Assess this cell for malaria.
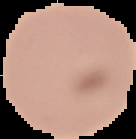

Uninfected.

Summary:
  - Preparation: thin blood film
  - Image type: segmented cell region with the area outside set to black
  - Image size: 136×139 pixels